Locate every Trypanosoma brucei.
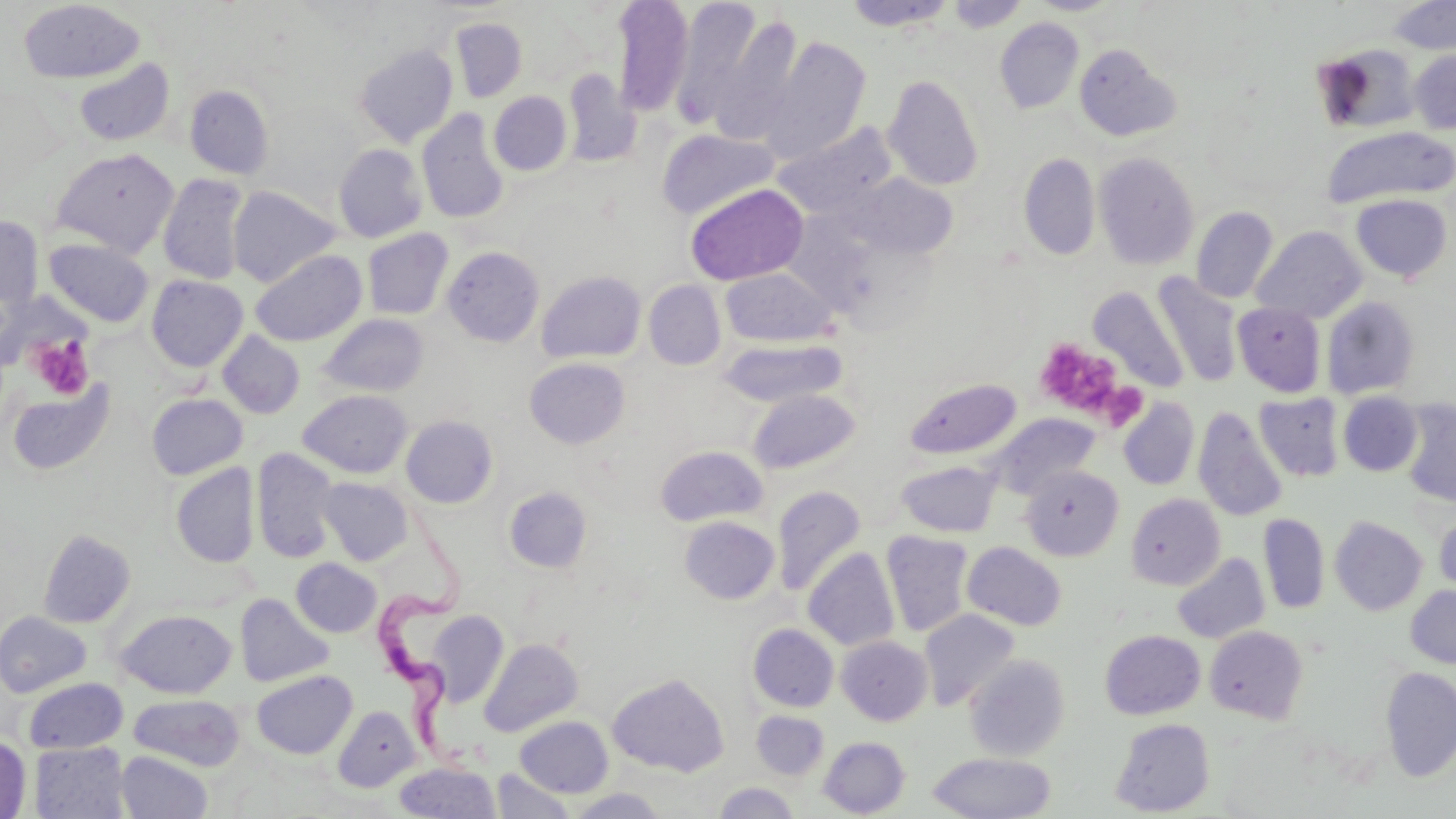

Approximate bounding boxes as (x1,y1)-(x2,y2) corner pairs in pixels.
Trypanosoma brucei: (358,494)-(476,766).

Summary:
  - Platelet locations: (28,335)-(94,399), (1035,337)-(1125,421)
  - Uninfected red blood cell locations: (611,0)-(694,116), (1028,0)-(1120,15), (1387,0)-(1456,55), (18,1)-(145,84), (671,1)-(767,127), (843,1)-(957,31), (946,1)-(1029,32), (710,13)-(804,142), (449,16)-(528,102), (994,17)-(1084,114), (761,36)-(872,163), (1073,43)-(1181,142), (1314,43)-(1422,133), (354,44)-(458,147), (1409,49)-(1456,134), (73,58)-(174,147), (562,70)-(640,166), (883,73)-(985,191), (184,85)-(274,179), (489,91)-(572,175), (417,109)-(510,224), (773,123)-(896,218), (1321,126)-(1455,209), (657,128)-(780,220), (333,143)-(427,243), (50,147)-(179,257), (1019,152)-(1101,260), (1094,152)-(1200,270), (158,173)-(249,285), (847,174)-(958,258), (685,183)-(808,285), (228,185)-(342,288), (1350,193)-(1453,282), (1191,206)-(1279,303), (0,215)-(44,310), (1251,225)-(1367,322), (362,228)-(454,321), (43,238)-(154,327), (442,246)-(544,347), (250,248)-(367,347), (721,267)-(837,347), (537,270)-(646,363), (1152,273)-(1243,387), (146,275)-(248,372), (643,280)-(726,370), (1088,286)-(1189,394), (1322,296)-(1420,399), (1232,303)-(1326,397), (318,313)-(430,398), (217,330)-(305,419), (719,338)-(849,408), (524,357)-(630,448), (904,378)-(1022,459), (6,380)-(117,475), (747,388)-(861,474), (298,389)-(413,477), (1338,391)-(1423,476), (146,393)-(248,480), (1255,393)-(1345,481), (1119,398)-(1200,490), (1398,398)-(1456,508), (1193,406)-(1288,522), (989,413)-(1099,497), (400,415)-(498,508), (655,445)-(768,526), (252,448)-(338,563), (896,460)-(1001,537), (171,464)-(259,568), (1020,464)-(1124,561), (319,477)-(414,565), (503,486)-(592,573), (772,486)-(866,597), (1126,493)-(1225,589), (1434,508)-(1456,596), (1258,513)-(1329,614), (679,516)-(779,604), (1330,516)-(1428,615), (38,529)-(135,628), (880,531)-(974,637), (962,542)-(1067,631), (803,547)-(899,651), (1172,553)-(1269,644), (291,558)-(381,637), (1405,585)-(1456,669), (235,594)-(333,687), (116,608)-(237,698), (919,608)-(1021,711), (0,611)-(92,697), (427,613)-(509,706), (748,623)-(838,712), (1204,625)-(1308,724), (1100,629)-(1205,719), (837,636)-(933,725), (480,638)-(582,736), (964,654)-(1070,761), (1379,667)-(1456,781), (251,670)-(357,759), (607,672)-(729,776), (24,678)-(128,754), (129,694)-(246,771), (333,705)-(420,791), (751,710)-(829,779), (514,715)-(613,797), (1110,718)-(1215,816), (0,734)-(31,819), (819,737)-(910,817), (29,742)-(130,819), (115,751)-(213,819), (926,751)-(1055,818), (394,762)-(500,818), (491,769)-(575,819), (712,782)-(801,818), (565,788)-(672,818)
  - Slide-level diagnosis: Trypanosoma brucei
  - Preparation: thin blood film
  - Image size: 1456×819 pixels
  - Magnification: 1000x
  - Field of view: one of a larger specimen
  - Stain: May-Grünwald-Giemsa
  - Modality: light microscopy